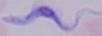
Summary:
  - Identification: trypanosome
  - Modality: photomicrograph
  - Magnification: 1000x